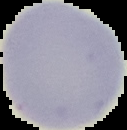
{
  "image_size": "127×130 pixels",
  "preparation": "thin blood smear",
  "malaria_status": "uninfected",
  "image_type": "segmented cell region with the area outside set to black"
}